Report the malaria status of this cell.
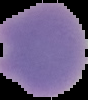
It is uninfected.

Summary:
  - Image size: 88×100 pixels
  - Preparation: thin blood film
  - Image type: segmented cell region on a black background